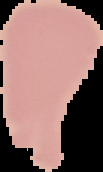
image type = segmented cell region on a black background
malaria status = uninfected
preparation = thin blood film
image size = 103×172 pixels